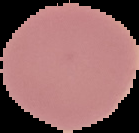
preparation = thin blood film
result = no Plasmodium parasites detected
image type = cell region segmented out of the field of view; surrounding area masked to black
image size = 139×133 pixels